Assess this cell for malaria.
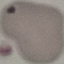

Uninfected.

image type = automatically extracted cell patch, resized to 64 × 64 pixels
capture = smartphone camera at the microscope eyepiece
preparation = thin blood film
stain = Giemsa